Outline each blood parasite and name the species.
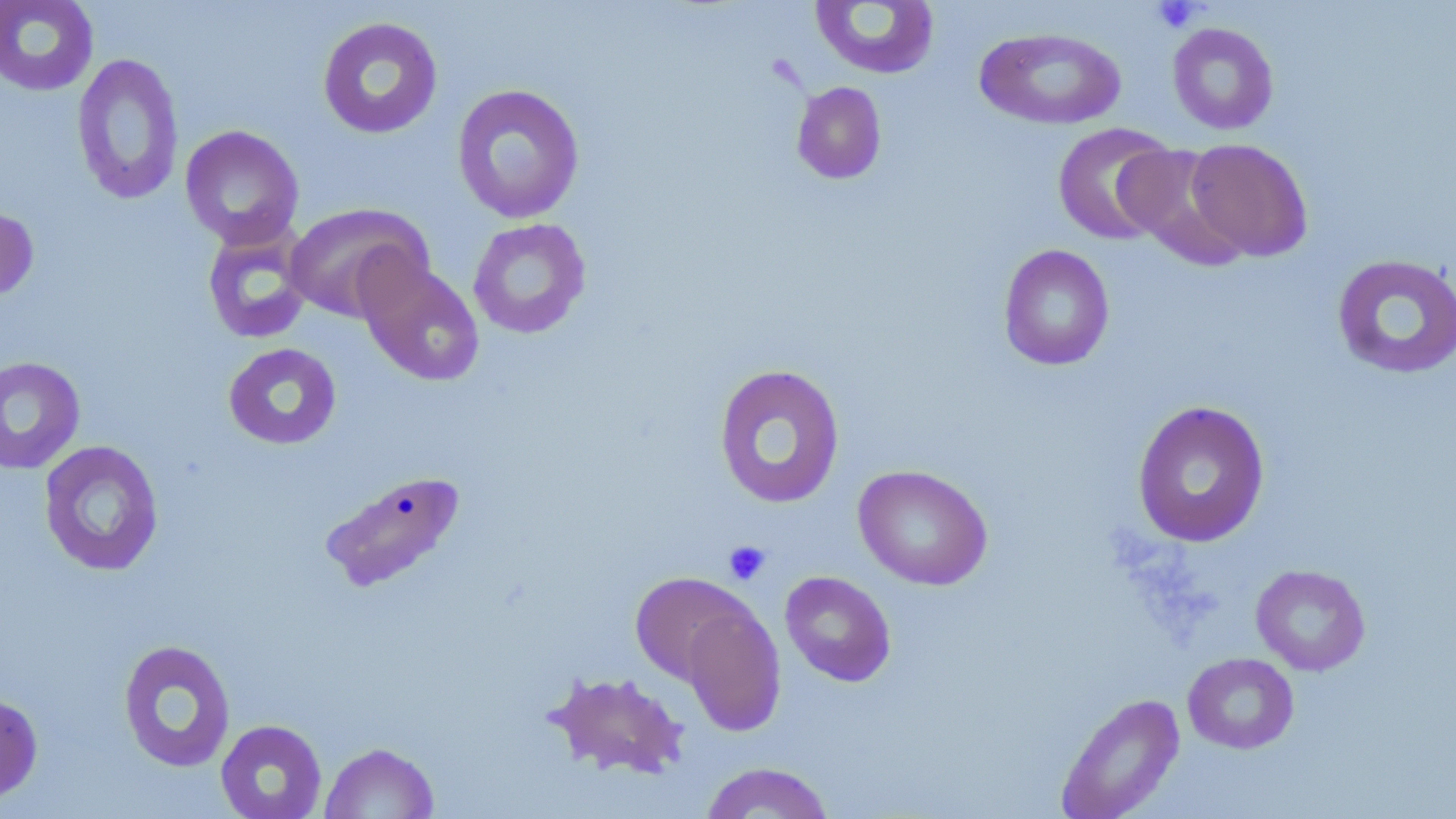

No blood parasites observed.

Approximate bounding boxes as [x1, y1, x2, y2] in pixels. Platelet locations: [1150, 1, 1204, 33], [722, 540, 771, 586]. Uninfected red blood cell locations: [0, 0, 99, 96], [809, 1, 940, 80], [317, 16, 443, 139], [1167, 22, 1279, 135], [974, 26, 1127, 130], [71, 52, 185, 206], [791, 81, 887, 185], [451, 83, 585, 224], [1052, 122, 1178, 245], [180, 125, 304, 248], [1184, 138, 1313, 262], [1117, 144, 1249, 269], [284, 202, 433, 324], [0, 205, 39, 302], [467, 218, 592, 340], [202, 224, 314, 344], [997, 244, 1115, 371], [1331, 253, 1456, 380], [357, 256, 485, 387], [223, 342, 342, 451], [0, 355, 85, 475], [712, 363, 846, 509], [1131, 400, 1270, 548], [38, 440, 165, 577], [852, 465, 993, 590], [326, 473, 465, 591], [1250, 564, 1371, 676], [780, 570, 897, 687], [629, 571, 756, 686], [680, 600, 785, 736], [117, 639, 237, 773], [1182, 652, 1299, 754], [544, 670, 691, 780], [0, 691, 43, 806], [1055, 692, 1185, 819], [215, 719, 327, 819], [319, 741, 439, 818], [699, 761, 836, 818]. Slide-level diagnosis: negative for blood parasites. Image is 1456×819 pixels. 1000x magnification. Thin blood smear. May-Grünwald-Giemsa stain. Light microscopy. One field of a larger specimen.